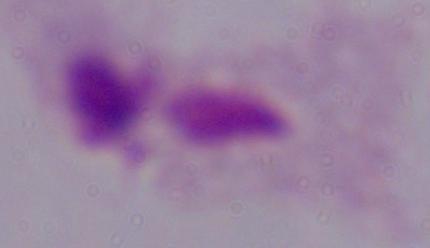
identification = trichomonad
magnification = 1000x
modality = photomicrograph